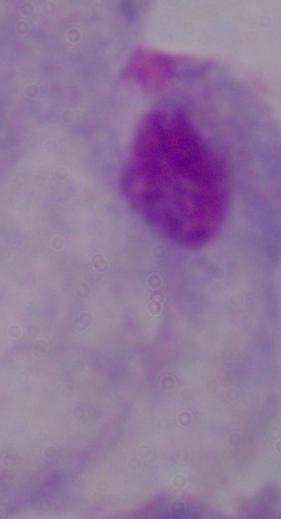

Summary:
  - Magnification: 1000x
  - Identification: trichomonad
  - Modality: photomicrograph